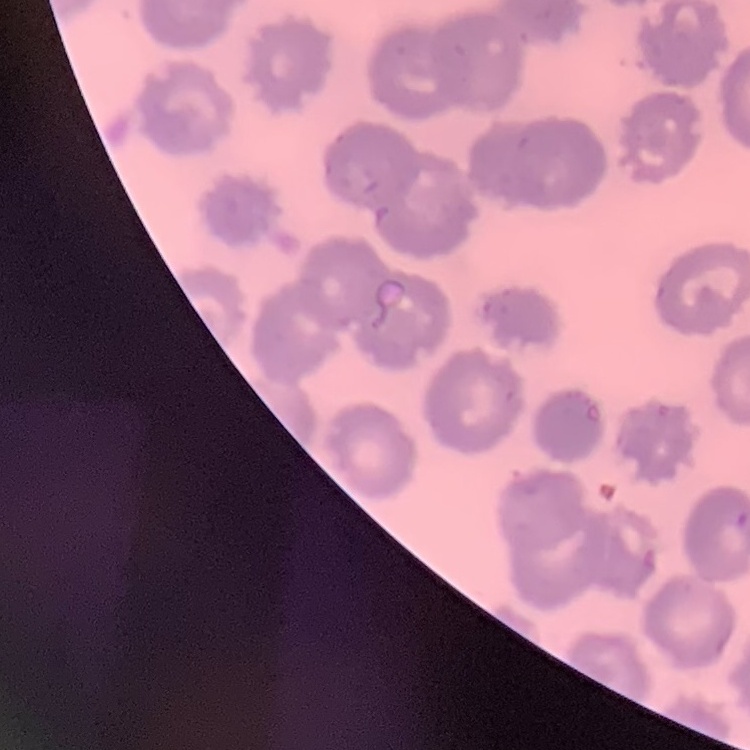 The red blood cells show no rouleaux formation. Thin blood smear. Stained with either Field's or Giemsa. Square crop of a larger photomicrograph.